State which cell type is depicted.
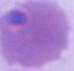
An erythrocyte.

Summary:
  - Modality: micrograph
  - Magnification: 1000x